Name the cell type shown.
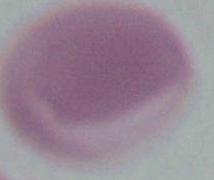
This is an erythrocyte.

Summary:
  - Magnification: 1000x
  - Modality: photomicrograph